State which cell type is depicted.
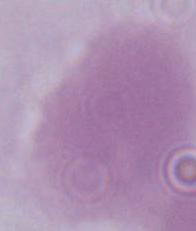

This is an erythrocyte.

magnification: 1000x
modality: micrograph